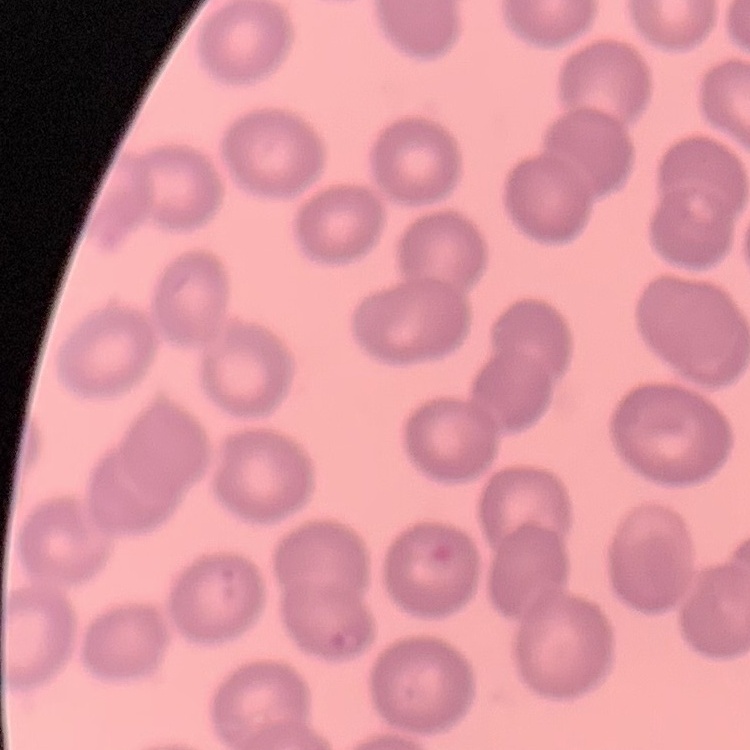
The red blood cells exhibit no rouleaux formation. Field's or Giemsa stain. Thin peripheral smear. One tile cut from a larger photomicrograph.